Classify this cell by malaria status.
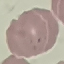
It is parasitized.

image type = cell patch, automatically extracted from a larger field of view and resized to 64 × 64 pixels
stain = Giemsa
preparation = thin smear
capture = smartphone through the microscope eyepiece